Identify the parasite.
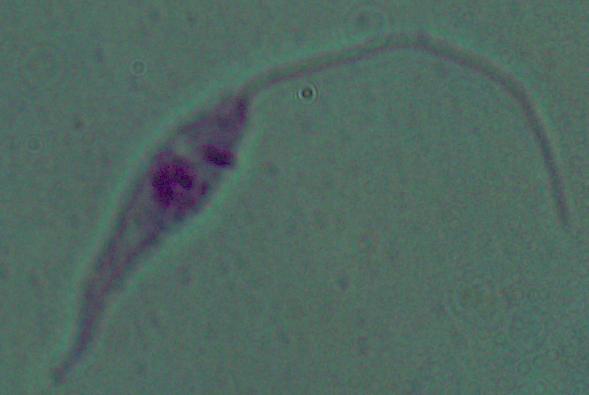

This is Leishmania.

Summary:
  - Modality: micrograph
  - Magnification: 1000x